Name the parasite shown.
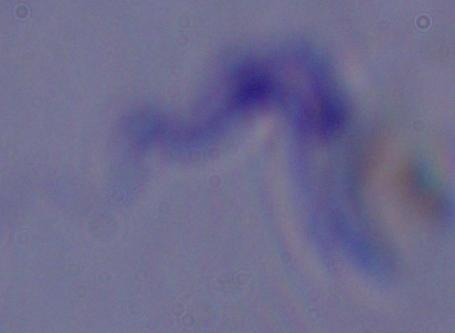

This is a trypanosome.

{
  "modality": "photomicrograph",
  "magnification": "1000x"
}